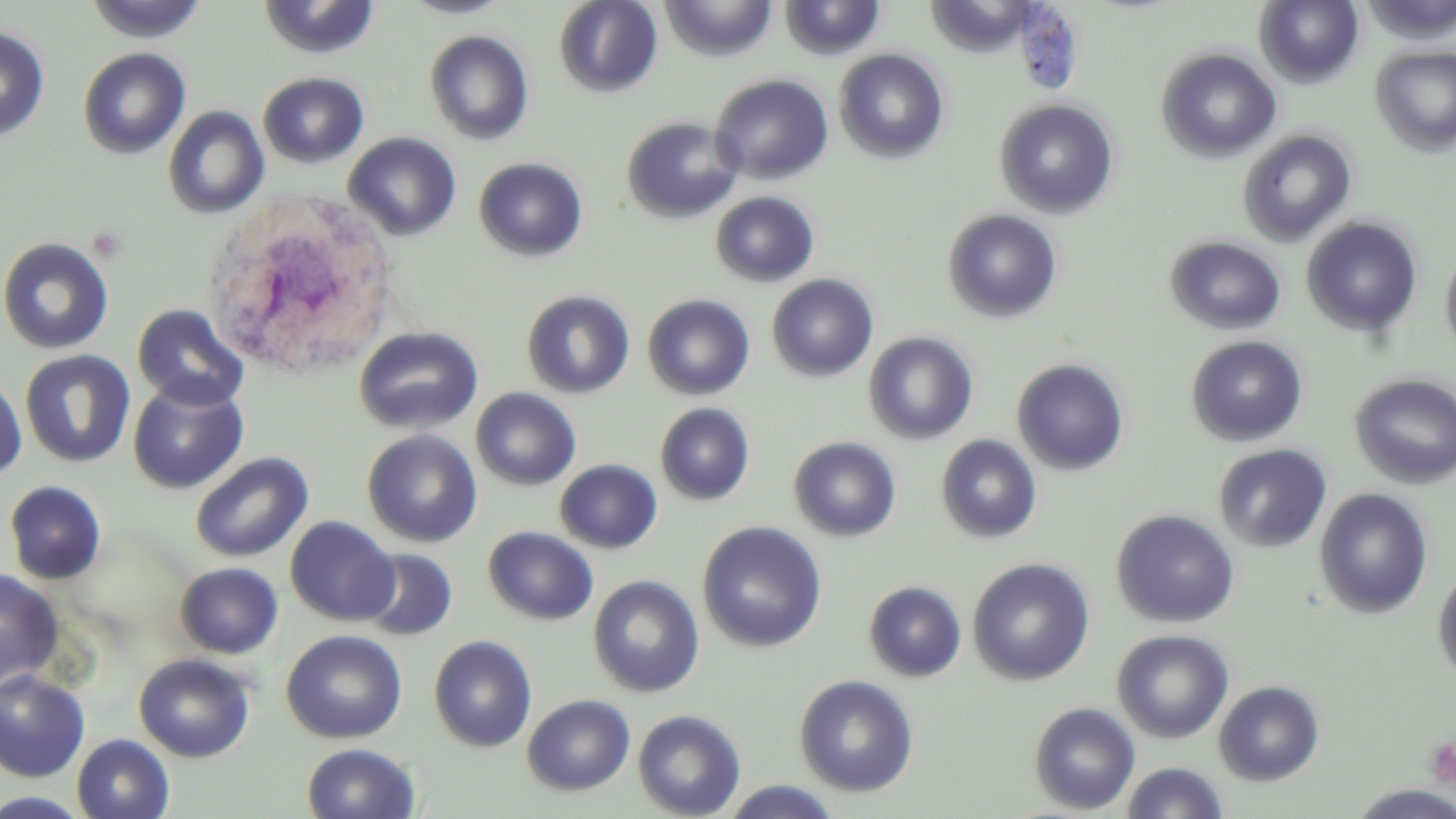

Approximate bounding boxes as named x1/y1/x2/y2 corners in pixels. Platelet locations: (x1=1426, y1=737, x2=1456, y2=789). White blood cell locations: (x1=204, y1=201, x2=396, y2=381). Uninfected red blood cell locations: (x1=84, y1=0, x2=209, y2=43), (x1=401, y1=0, x2=513, y2=19), (x1=554, y1=0, x2=662, y2=97), (x1=661, y1=0, x2=777, y2=60), (x1=780, y1=0, x2=886, y2=61), (x1=1256, y1=0, x2=1364, y2=86), (x1=258, y1=1, x2=382, y2=60), (x1=0, y1=25, x2=50, y2=142), (x1=424, y1=29, x2=534, y2=145), (x1=1372, y1=45, x2=1456, y2=155), (x1=78, y1=47, x2=191, y2=160), (x1=1157, y1=48, x2=1280, y2=162), (x1=834, y1=49, x2=949, y2=164), (x1=258, y1=71, x2=369, y2=169), (x1=709, y1=74, x2=834, y2=185), (x1=995, y1=98, x2=1119, y2=218), (x1=163, y1=105, x2=270, y2=219), (x1=622, y1=116, x2=744, y2=223), (x1=1238, y1=129, x2=1357, y2=247), (x1=344, y1=132, x2=462, y2=240), (x1=474, y1=157, x2=588, y2=262), (x1=710, y1=191, x2=820, y2=288), (x1=943, y1=208, x2=1063, y2=323), (x1=1302, y1=217, x2=1423, y2=337), (x1=1166, y1=235, x2=1286, y2=335), (x1=0, y1=236, x2=114, y2=354), (x1=1440, y1=247, x2=1456, y2=362), (x1=767, y1=274, x2=879, y2=382), (x1=522, y1=290, x2=635, y2=398), (x1=642, y1=294, x2=756, y2=400), (x1=132, y1=304, x2=249, y2=412), (x1=353, y1=325, x2=483, y2=435), (x1=863, y1=331, x2=979, y2=445), (x1=1186, y1=335, x2=1308, y2=447), (x1=20, y1=349, x2=135, y2=468), (x1=1012, y1=358, x2=1129, y2=475), (x1=1350, y1=373, x2=1456, y2=488), (x1=0, y1=374, x2=27, y2=482), (x1=128, y1=378, x2=248, y2=494), (x1=471, y1=387, x2=581, y2=491), (x1=655, y1=403, x2=755, y2=505), (x1=362, y1=430, x2=482, y2=547), (x1=936, y1=434, x2=1042, y2=543), (x1=789, y1=436, x2=901, y2=542), (x1=1214, y1=443, x2=1332, y2=553), (x1=190, y1=451, x2=314, y2=563), (x1=555, y1=459, x2=662, y2=554), (x1=3, y1=480, x2=108, y2=585), (x1=1314, y1=488, x2=1434, y2=619), (x1=1111, y1=508, x2=1240, y2=628), (x1=285, y1=515, x2=399, y2=626), (x1=698, y1=521, x2=827, y2=652), (x1=484, y1=526, x2=599, y2=626), (x1=358, y1=547, x2=458, y2=641), (x1=968, y1=558, x2=1094, y2=686), (x1=174, y1=562, x2=283, y2=659), (x1=1432, y1=565, x2=1456, y2=687), (x1=0, y1=569, x2=64, y2=691), (x1=588, y1=575, x2=704, y2=697), (x1=864, y1=581, x2=967, y2=682), (x1=281, y1=629, x2=407, y2=743), (x1=1112, y1=629, x2=1234, y2=744), (x1=428, y1=635, x2=538, y2=752), (x1=134, y1=653, x2=255, y2=763), (x1=0, y1=669, x2=90, y2=782), (x1=794, y1=675, x2=919, y2=797), (x1=1213, y1=680, x2=1325, y2=785), (x1=522, y1=694, x2=635, y2=796), (x1=1029, y1=702, x2=1140, y2=814), (x1=633, y1=709, x2=746, y2=819), (x1=71, y1=734, x2=175, y2=819), (x1=302, y1=742, x2=421, y2=819), (x1=1121, y1=761, x2=1230, y2=818), (x1=720, y1=780, x2=843, y2=819), (x1=1348, y1=785, x2=1456, y2=819), (x1=0, y1=791, x2=93, y2=818). Slide-level diagnosis: no evidence of blood parasites. Single field of view. Image is 1456×819 pixels. Thin blood film. Optical microscopy. May-Grünwald-Giemsa stain. Captured at 1000x magnification.